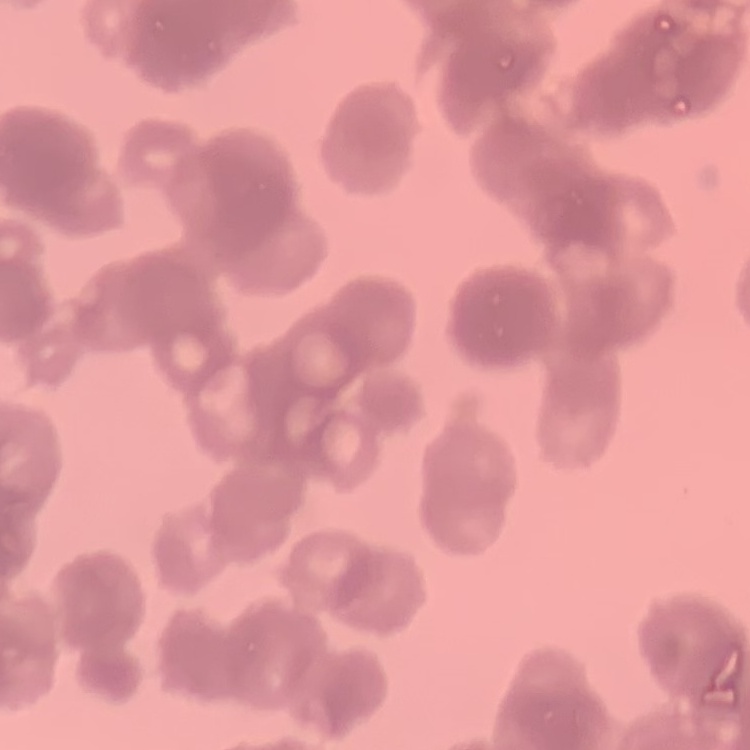
Summary:
  - Erythrocyte morphology: rouleaux formation
  - Preparation: thin blood film
  - Stain: Field's or Giemsa
  - Image type: one tile cut from a larger photomicrograph